Assess the morphology of the red blood cells.
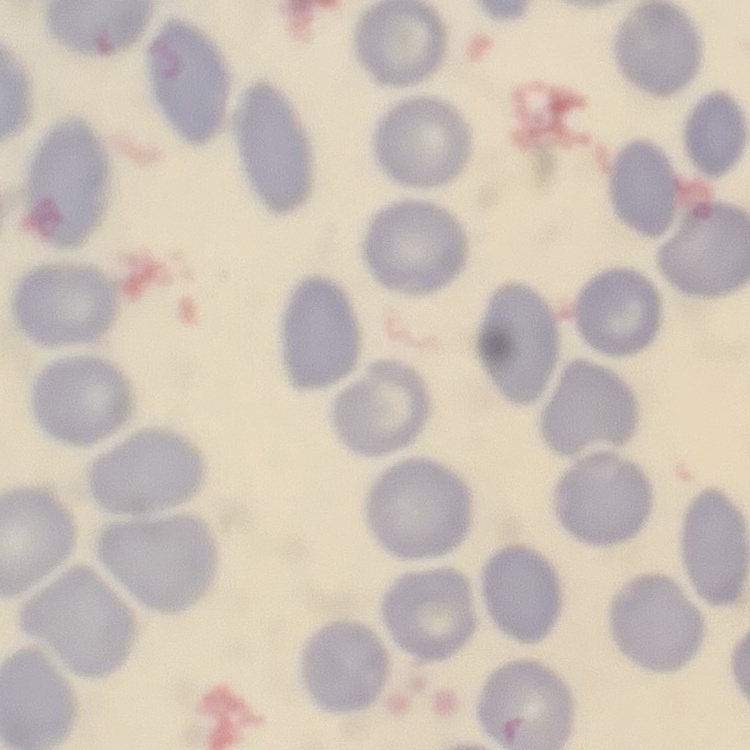
They show no rouleaux formation.

Field's or Giemsa stain. Thin blood film. Square crop of a larger photomicrograph.